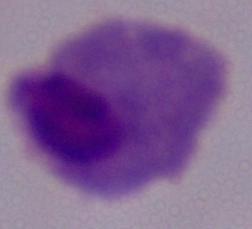

1000x magnification. A trichomonad is seen. Micrograph.